Describe the morphology of the red blood cells.
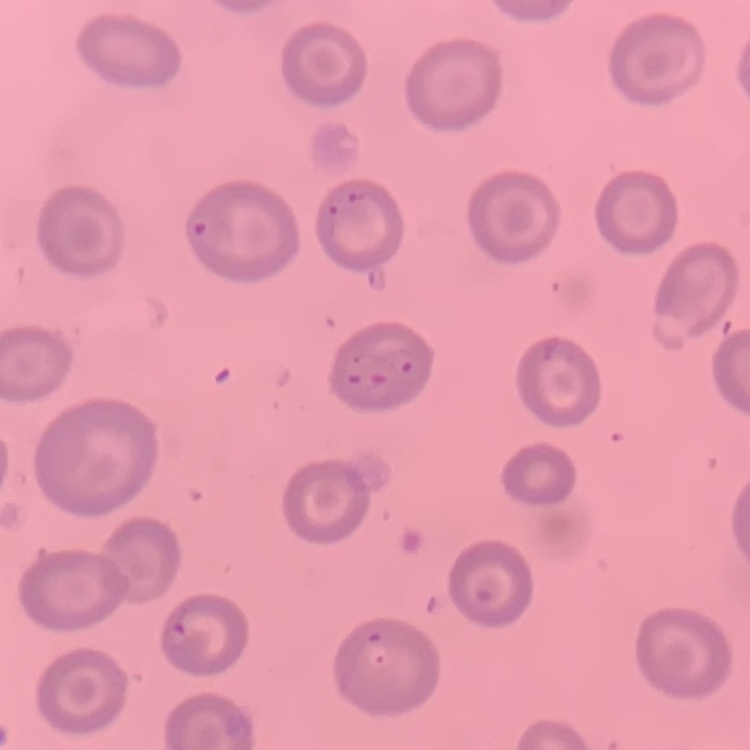

No rouleaux formation.

Summary:
  - Image type: one tile cut from a larger photomicrograph
  - Preparation: thin blood smear
  - Stain: Field's or Giemsa